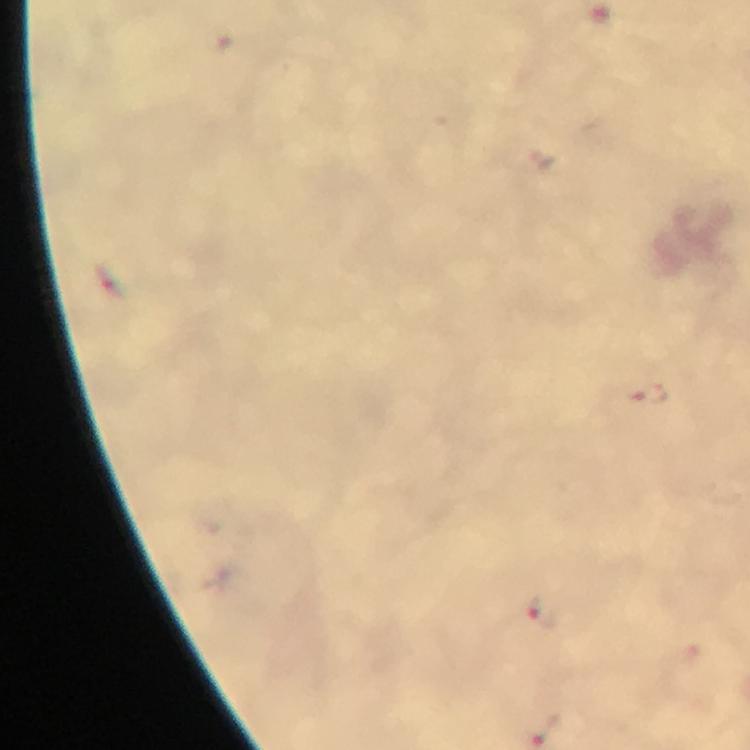
cropped from = one field of view
capture = smartphone photograph through a microscope
preparation = thick smear
image size = 750×750 pixels
magnification = 100x
context = from a diagnostic examination for malaria
immersion oil = used
malaria parasite locations = approximate centers as {x, y} in pixels: {648, 394}, {541, 615}
stain = Giemsa